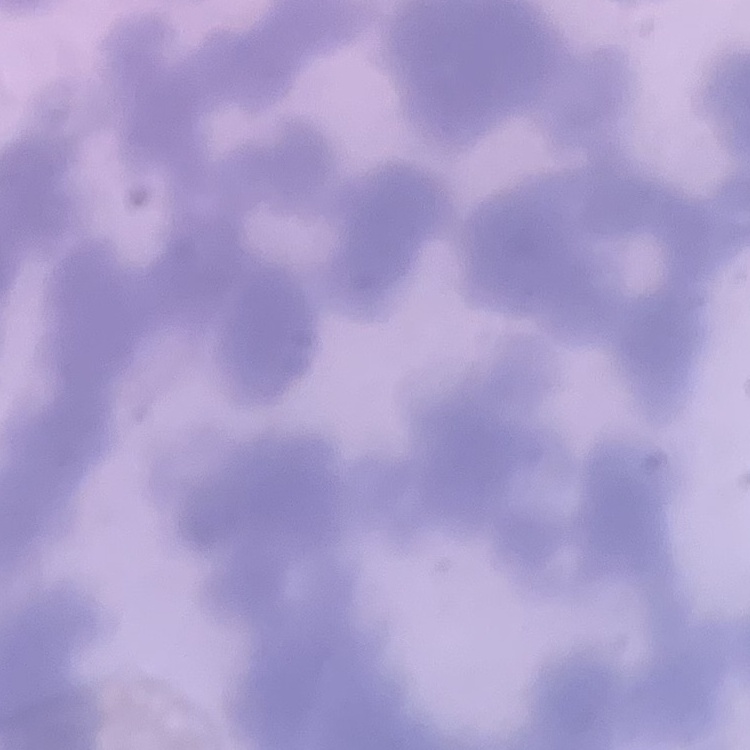

The erythrocytes show rouleaux formation. Stained with either Field's or Giemsa. Square crop of a larger photomicrograph. Thin blood smear.